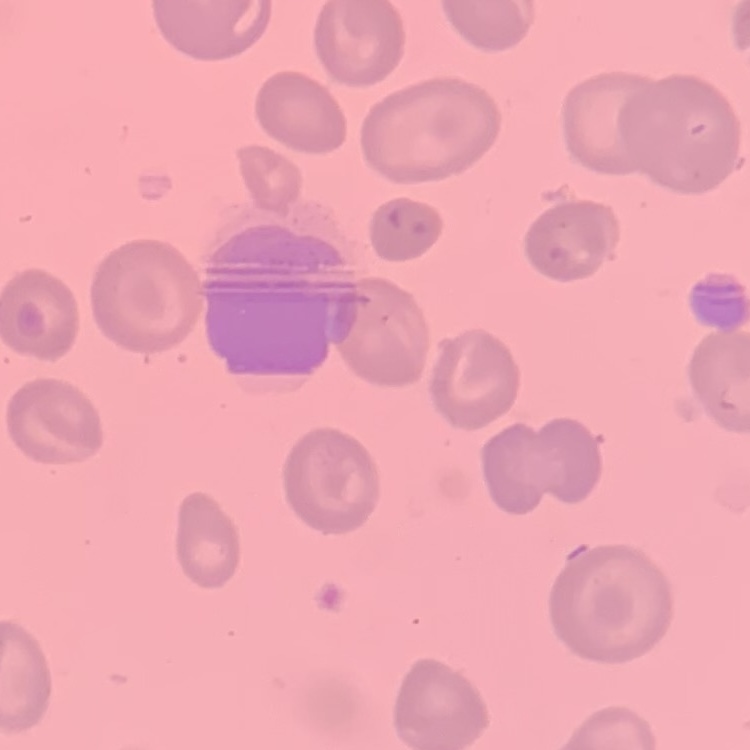
Summary:
  - Erythrocyte morphology: no rouleaux formation
  - Stain: Field's or Giemsa
  - Image type: one tile cut from a larger photomicrograph
  - Preparation: thin blood smear